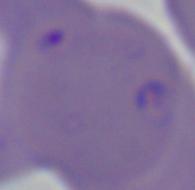

Summary:
  - Identification: Babesia
  - Magnification: 1000x
  - Modality: photomicrograph